Assess this cell for malaria.
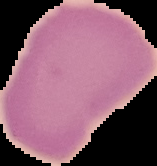
Uninfected.

image_size: 157×166 pixels
image_type: cell region segmented out of the field of view; surrounding area masked to black
preparation: thin blood film